Assess the morphology of the red blood cells.
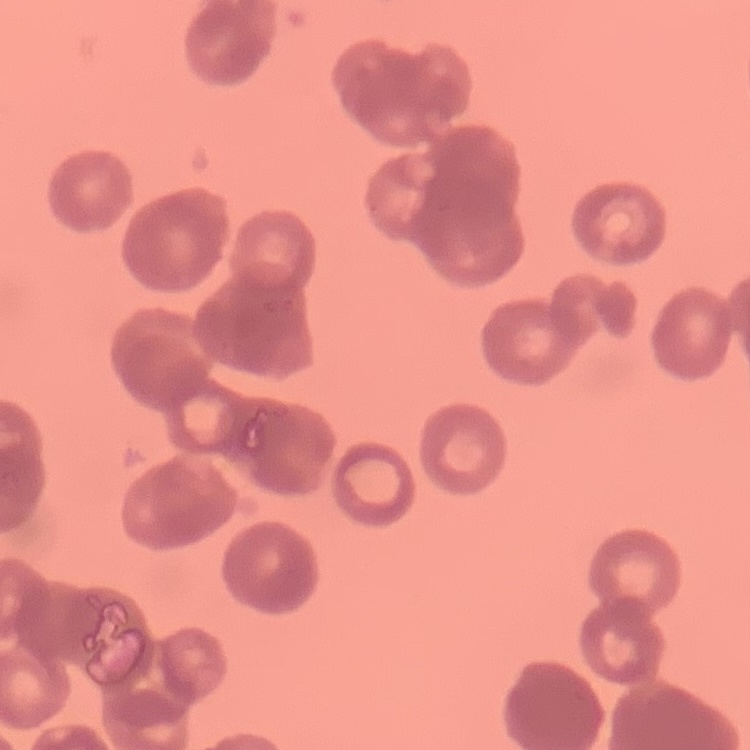

They show rouleaux formation.

Field's or Giemsa stain. One tile cut from a larger photomicrograph. Thin blood film.